State which parasite is depicted.
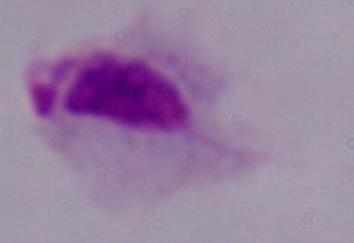

This is a trichomonad.

Summary:
  - Magnification: 1000x
  - Modality: micrograph